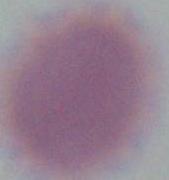
Summary:
  - Magnification: 1000x
  - Modality: micrograph
  - Identification: red blood cell